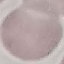
Summary:
  - Malaria status: uninfected
  - Image type: automatically extracted cell patch, resized to 64 × 64 pixels
  - Stain: Giemsa
  - Capture: smartphone through the microscope eyepiece
  - Preparation: thin blood film